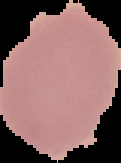
malaria status = uninfected
image type = segmented cell region on a black background
preparation = thin blood film
image size = 121×163 pixels